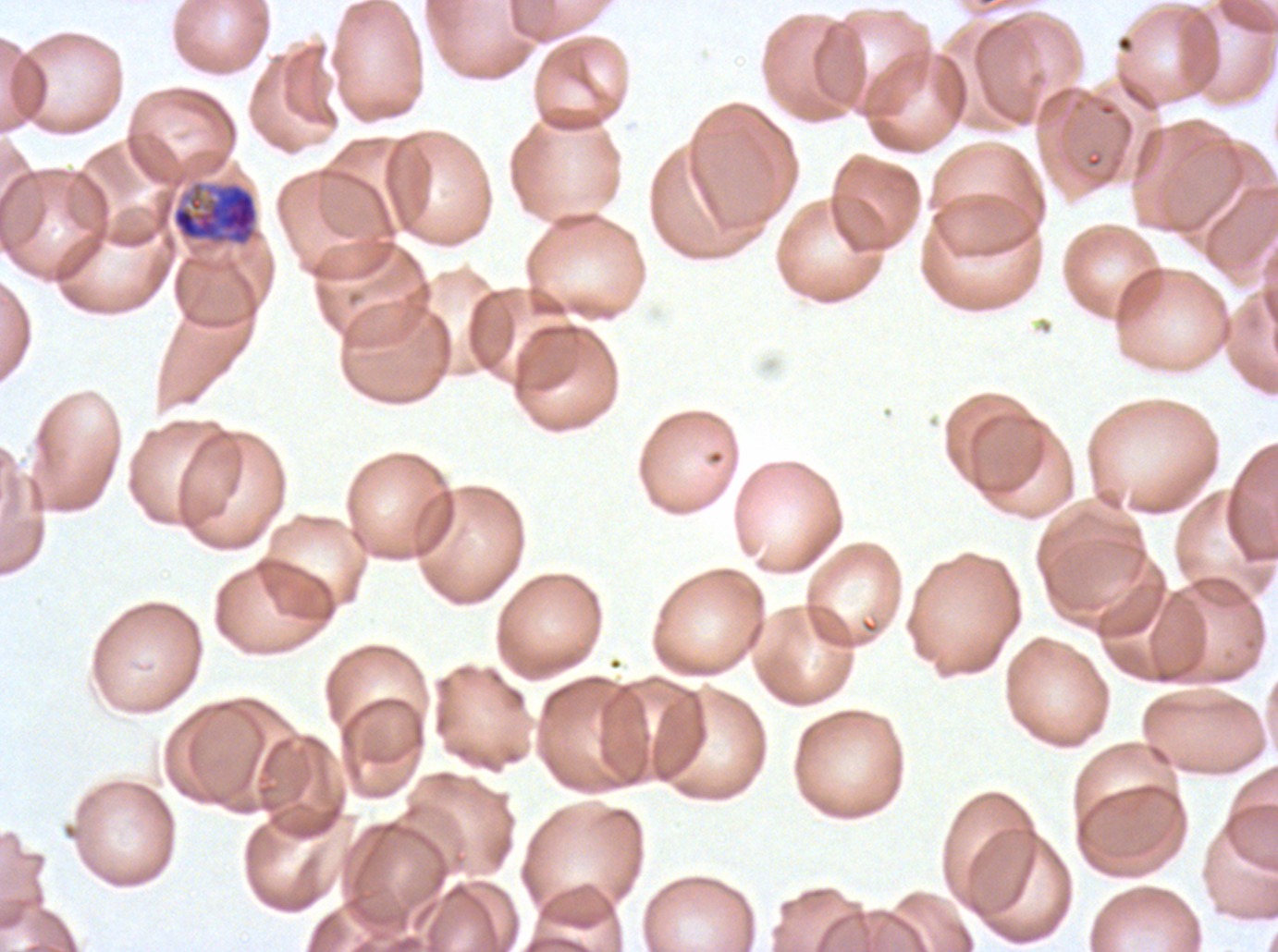

Approximate bounding boxes as [x1, y1, x2, y2] in pixels.
Summary:
  - Early schizont locations: [171, 180, 259, 247]
  - Image size: 1278×952 pixels
  - Stain: Giemsa
  - Preparation: thin blood smear
  - Specimen: P. falciparum cultured ex vivo for 24 to 48 hours, from a patient in The Gambia
  - Field of view: one sub-image of a larger composite